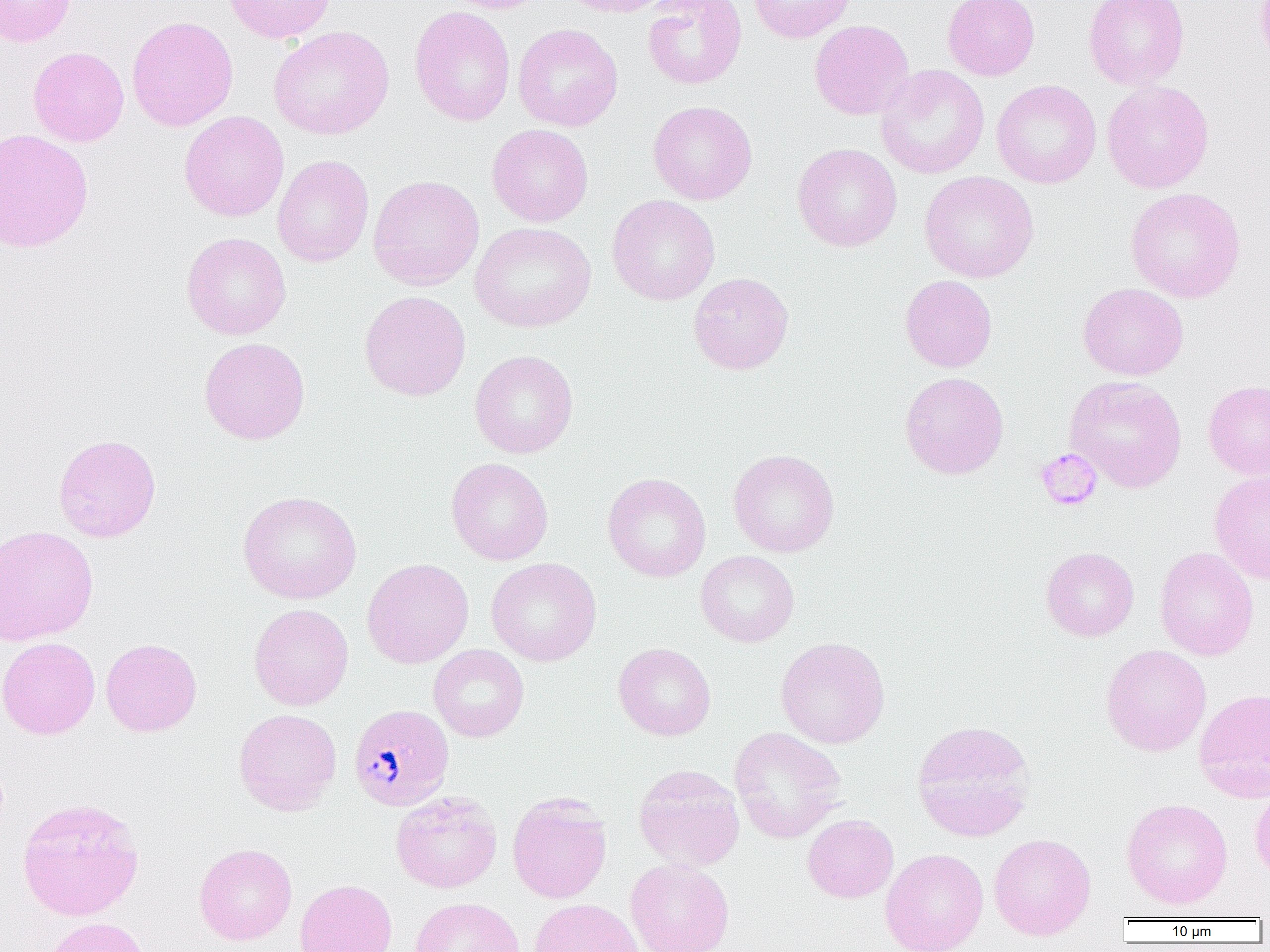
Summary:
  - Coordinate format: approximate bounding boxes as [x1, y1, x2, y2] in pixels
  - Platelet locations: [1035, 448, 1102, 510]
  - Plasmodium malariae-infected red blood cell locations: [348, 703, 455, 811]
  - Uninfected red blood cell locations: [0, 0, 75, 46], [223, 0, 336, 43], [442, 0, 551, 14], [556, 0, 674, 17], [642, 0, 746, 90], [748, 0, 856, 43], [943, 0, 1040, 80], [1084, 0, 1189, 90], [409, 6, 516, 126], [126, 15, 239, 131], [809, 19, 914, 120], [512, 23, 623, 131], [268, 25, 395, 140], [28, 46, 129, 147], [875, 64, 990, 179], [991, 79, 1101, 188], [1101, 80, 1214, 193], [648, 100, 757, 205], [179, 111, 289, 221], [487, 124, 594, 227], [0, 128, 94, 252], [792, 143, 902, 252], [272, 155, 374, 267], [919, 171, 1039, 283], [368, 174, 485, 291], [1125, 187, 1246, 303], [607, 194, 720, 306], [470, 222, 596, 332], [181, 232, 291, 340], [688, 272, 794, 375], [900, 274, 997, 372], [1078, 282, 1189, 380], [359, 290, 471, 401], [199, 337, 310, 444], [469, 349, 579, 458], [899, 371, 1009, 479], [1065, 376, 1187, 493], [1203, 379, 1270, 479], [53, 433, 161, 542], [728, 448, 840, 558], [446, 457, 554, 565], [1209, 470, 1270, 584], [602, 472, 712, 582], [238, 490, 362, 604], [0, 525, 98, 646], [1041, 546, 1139, 641], [1154, 547, 1259, 660], [695, 550, 799, 647], [486, 557, 602, 666], [362, 558, 474, 669], [248, 603, 354, 710], [775, 636, 890, 749], [0, 637, 100, 739], [101, 638, 202, 737], [613, 642, 716, 740], [428, 644, 529, 742], [1101, 644, 1212, 756], [1194, 688, 1270, 802], [233, 708, 342, 816], [911, 720, 1036, 841], [729, 726, 847, 843], [633, 764, 745, 871], [1250, 785, 1270, 883], [391, 791, 502, 893], [508, 793, 612, 903], [17, 798, 144, 920], [1121, 798, 1233, 909], [802, 814, 899, 903], [989, 833, 1096, 940], [194, 843, 297, 945], [880, 848, 989, 952], [625, 858, 734, 952], [295, 879, 397, 952], [410, 897, 525, 952], [529, 898, 644, 952], [40, 917, 150, 952]
  - Slide-level diagnosis: Plasmodium malariae
  - Image size: 1270×952 pixels
  - Field of view: single
  - Preparation: thin blood smear
  - Magnification: 1000x
  - Modality: light microscopy